Assess for Plasmodium parasites.
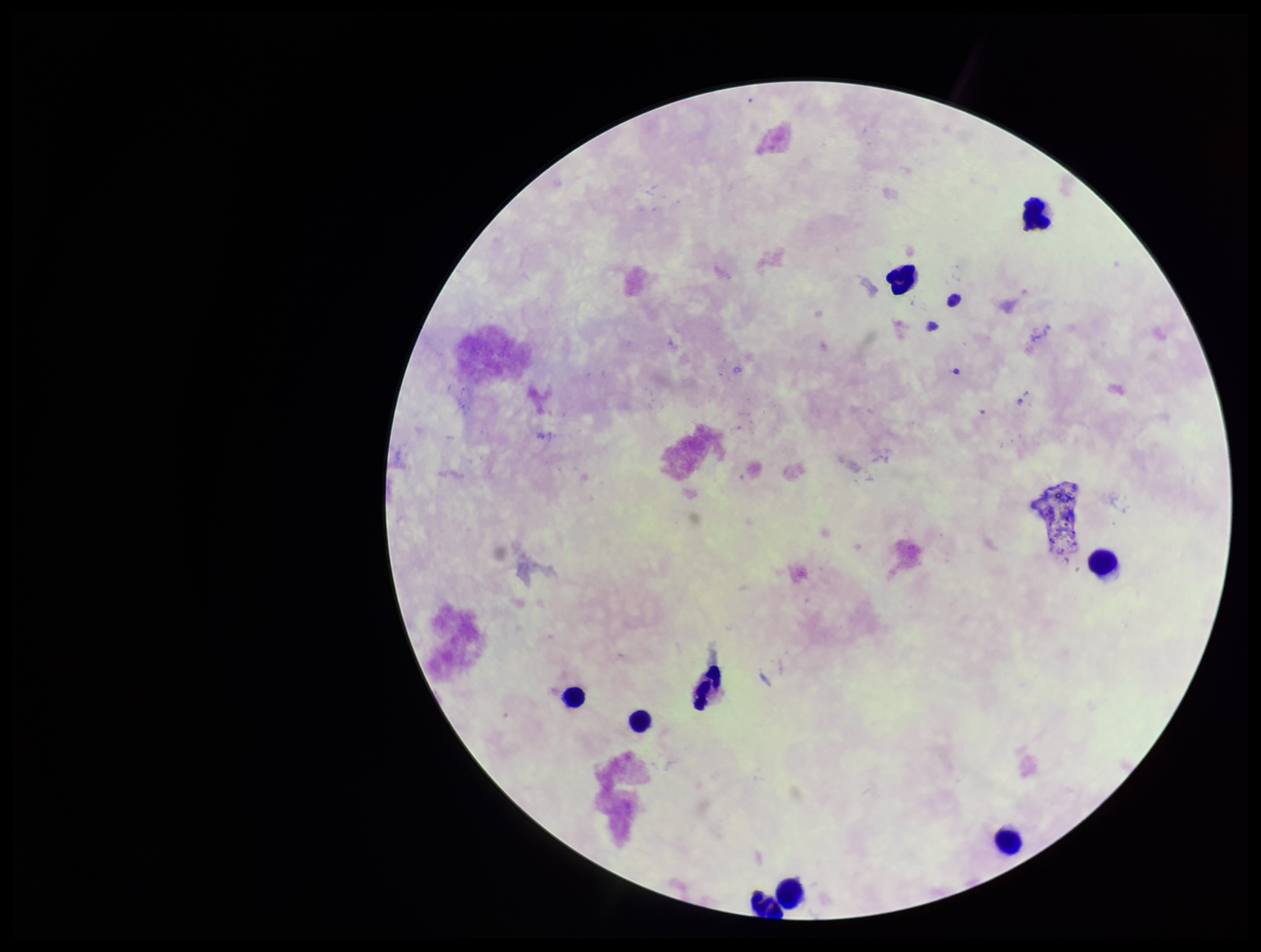

None identified.

{
  "parasite_count": 0,
  "preparation": "thick blood smear",
  "leukocyte_count": 9,
  "field_of_view": "single",
  "stain": "Giemsa",
  "image_size": "1261×952 pixels",
  "capture": "smartphone photograph through the microscope eyepiece",
  "patient_malaria_status": "negative"
}